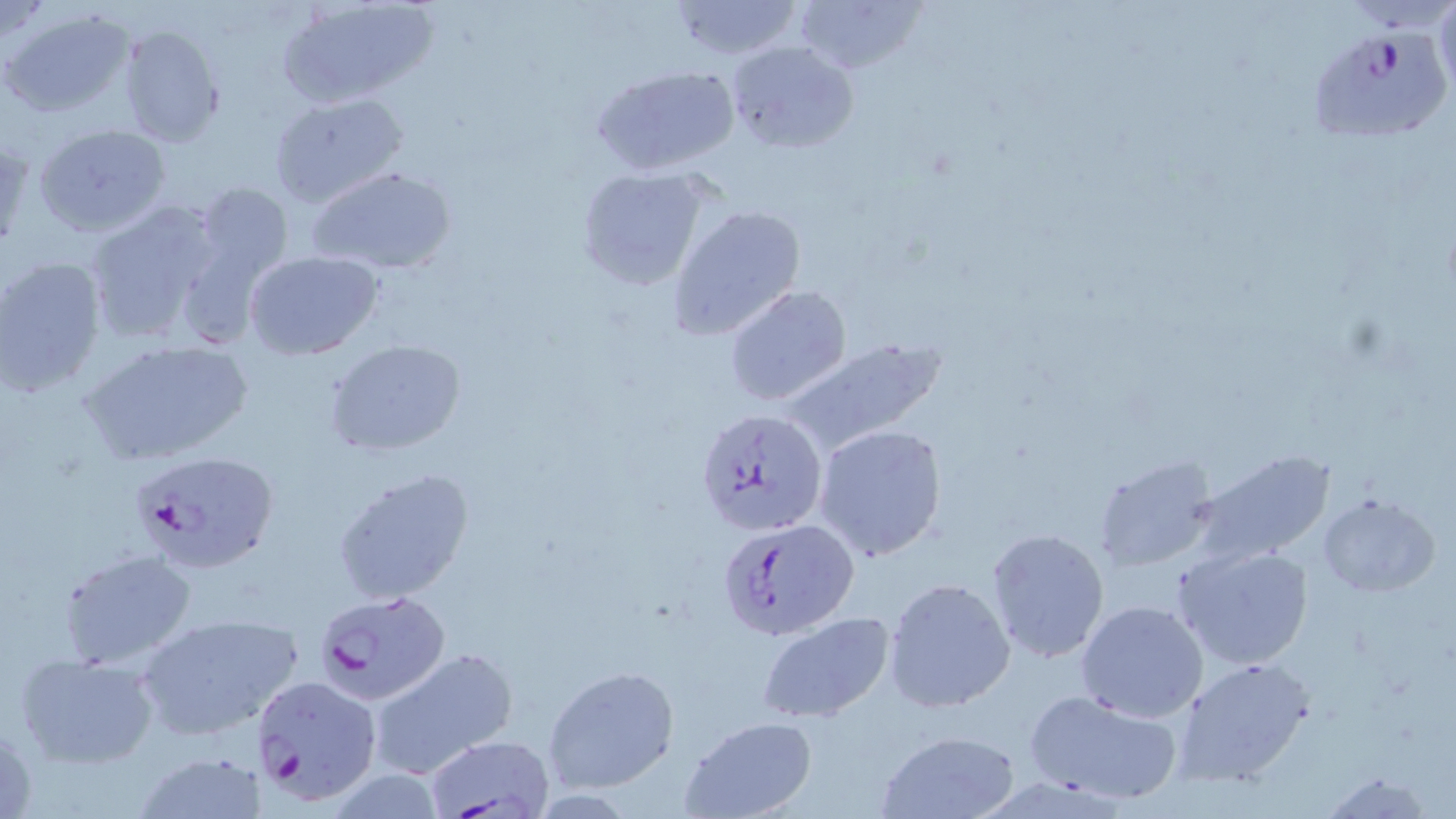
slide-level diagnosis = Plasmodium falciparum
field of view = single
uninfected red blood cell locations = approximate bounding boxes as named x1/y1/x2/y2 corners in pixels: (x1=666, y1=0, x2=805, y2=61), (x1=795, y1=0, x2=926, y2=77), (x1=1435, y1=0, x2=1456, y2=98), (x1=279, y1=1, x2=434, y2=105), (x1=2, y1=7, x2=133, y2=118), (x1=118, y1=25, x2=224, y2=145), (x1=723, y1=39, x2=857, y2=154), (x1=589, y1=64, x2=740, y2=176), (x1=268, y1=91, x2=409, y2=209), (x1=36, y1=126, x2=171, y2=237), (x1=310, y1=166, x2=455, y2=275), (x1=575, y1=167, x2=714, y2=292), (x1=192, y1=181, x2=294, y2=287), (x1=82, y1=200, x2=227, y2=347), (x1=668, y1=204, x2=806, y2=341), (x1=245, y1=250, x2=384, y2=359), (x1=0, y1=256, x2=108, y2=397), (x1=724, y1=285, x2=852, y2=407), (x1=778, y1=338, x2=948, y2=454), (x1=323, y1=339, x2=468, y2=457), (x1=83, y1=340, x2=253, y2=466), (x1=815, y1=424, x2=948, y2=562), (x1=1194, y1=450, x2=1335, y2=565), (x1=1092, y1=453, x2=1219, y2=572), (x1=331, y1=466, x2=475, y2=606), (x1=1318, y1=493, x2=1440, y2=595), (x1=985, y1=527, x2=1110, y2=664), (x1=1174, y1=543, x2=1315, y2=671), (x1=59, y1=548, x2=196, y2=669), (x1=883, y1=577, x2=1016, y2=712), (x1=1074, y1=599, x2=1209, y2=723), (x1=135, y1=609, x2=306, y2=740), (x1=754, y1=613, x2=897, y2=724), (x1=367, y1=647, x2=517, y2=779), (x1=16, y1=653, x2=161, y2=769), (x1=1172, y1=656, x2=1315, y2=788), (x1=543, y1=666, x2=679, y2=793), (x1=1025, y1=688, x2=1184, y2=805), (x1=679, y1=717, x2=816, y2=819), (x1=874, y1=730, x2=1025, y2=819), (x1=135, y1=750, x2=269, y2=819), (x1=1317, y1=770, x2=1437, y2=818)
magnification = 1000x
Plasmodium falciparum-infected red blood cell locations = approximate bounding boxes as named x1/y1/x2/y2 corners in pixels: (x1=1307, y1=27, x2=1455, y2=146), (x1=696, y1=409, x2=828, y2=535), (x1=130, y1=449, x2=280, y2=575), (x1=717, y1=517, x2=860, y2=641), (x1=313, y1=590, x2=453, y2=705), (x1=250, y1=673, x2=382, y2=805), (x1=427, y1=737, x2=551, y2=816)
stain = May-Grünwald-Giemsa
modality = light microscopy
image size = 1456×819 pixels
preparation = thin blood smear